State the preparation type.
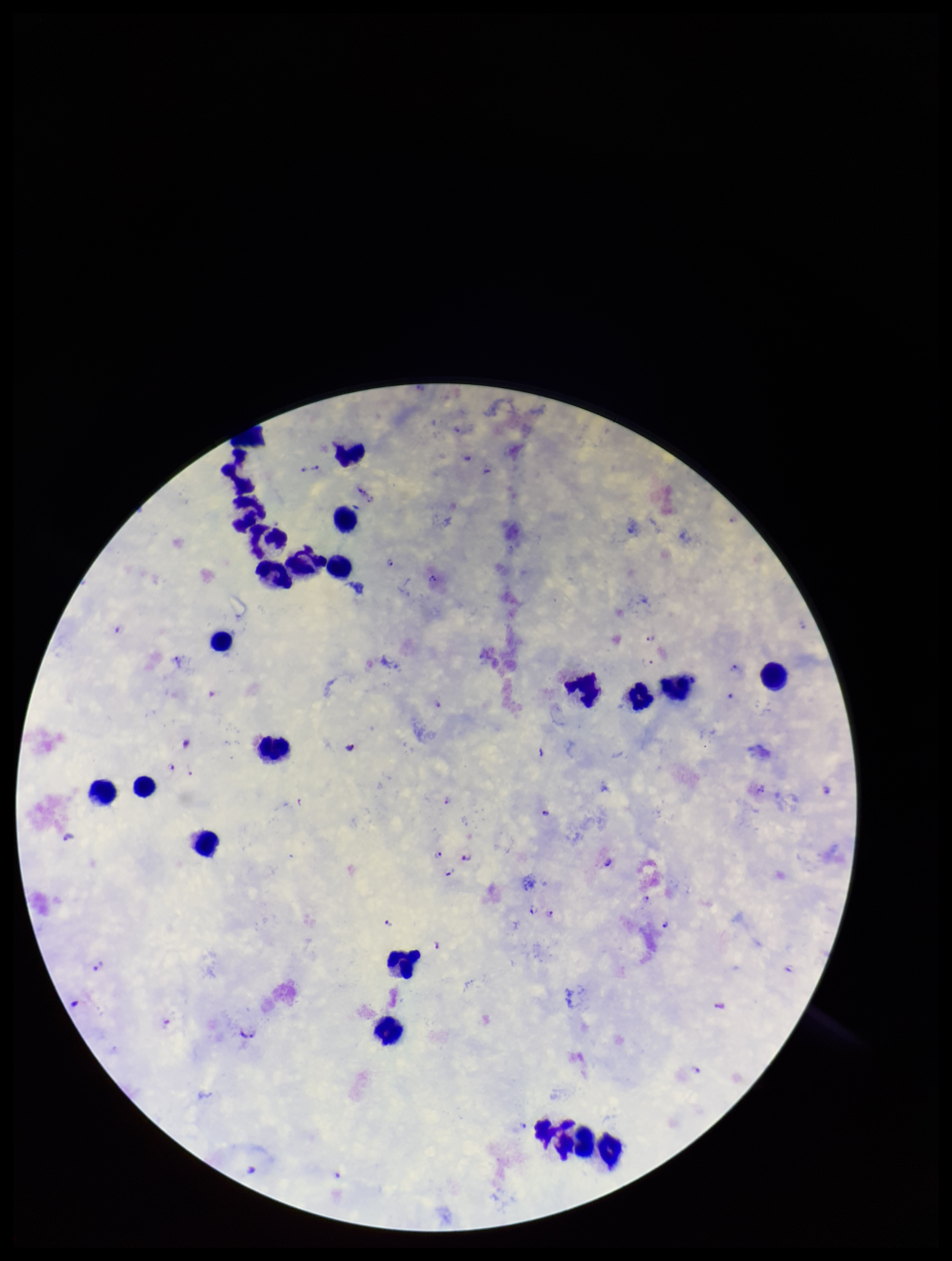

Thick.

capture = smartphone photograph through the microscope eyepiece
leukocyte count = 22
Plasmodium parasites = seen
species reported for this patient = Plasmodium falciparum
patient malaria status = infected
parasite count = 28
image size = 952×1261 pixels
field of view = one from this slide
stain = Giemsa